Locate leukocytes (white blood cells).
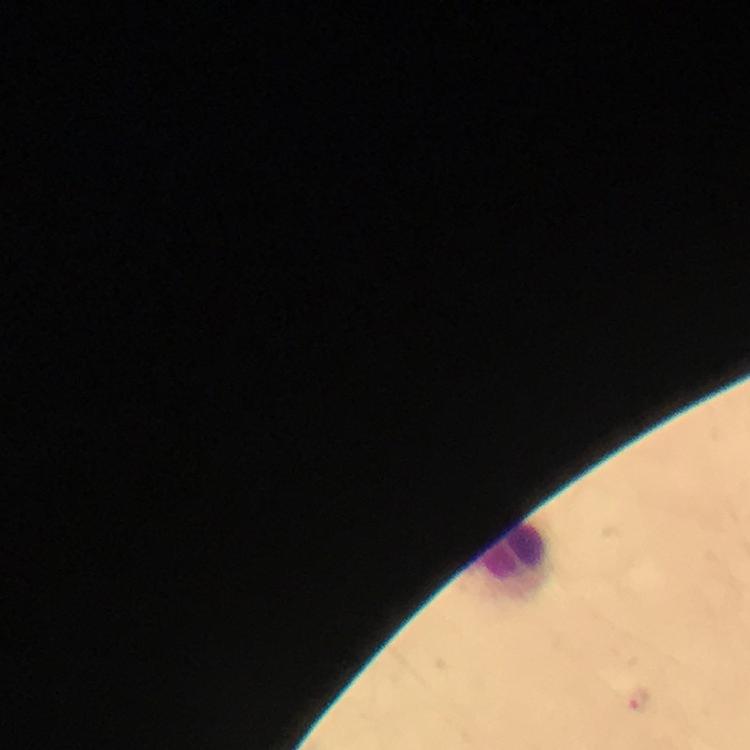
Approximate centers as (x, y) in pixels.
Leukocytes: (516, 558).

Summary:
  - Image size: 750×750 pixels
  - Magnification: 100x
  - Stain: Giemsa
  - Malaria parasites: none seen
  - Cropped from: a single field of view
  - Immersion oil: used
  - Preparation: thick blood film
  - Context: from a diagnostic examination for malaria
  - Capture: smartphone camera through the microscope